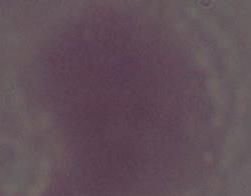 An erythrocyte is seen. Photomicrograph. 1000x magnification.